Report the malaria status of this cell.
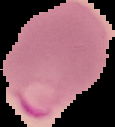

It is parasitized.

Summary:
  - Image size: 115×127 pixels
  - Image type: segmented cell region on a black background
  - Preparation: thin blood film